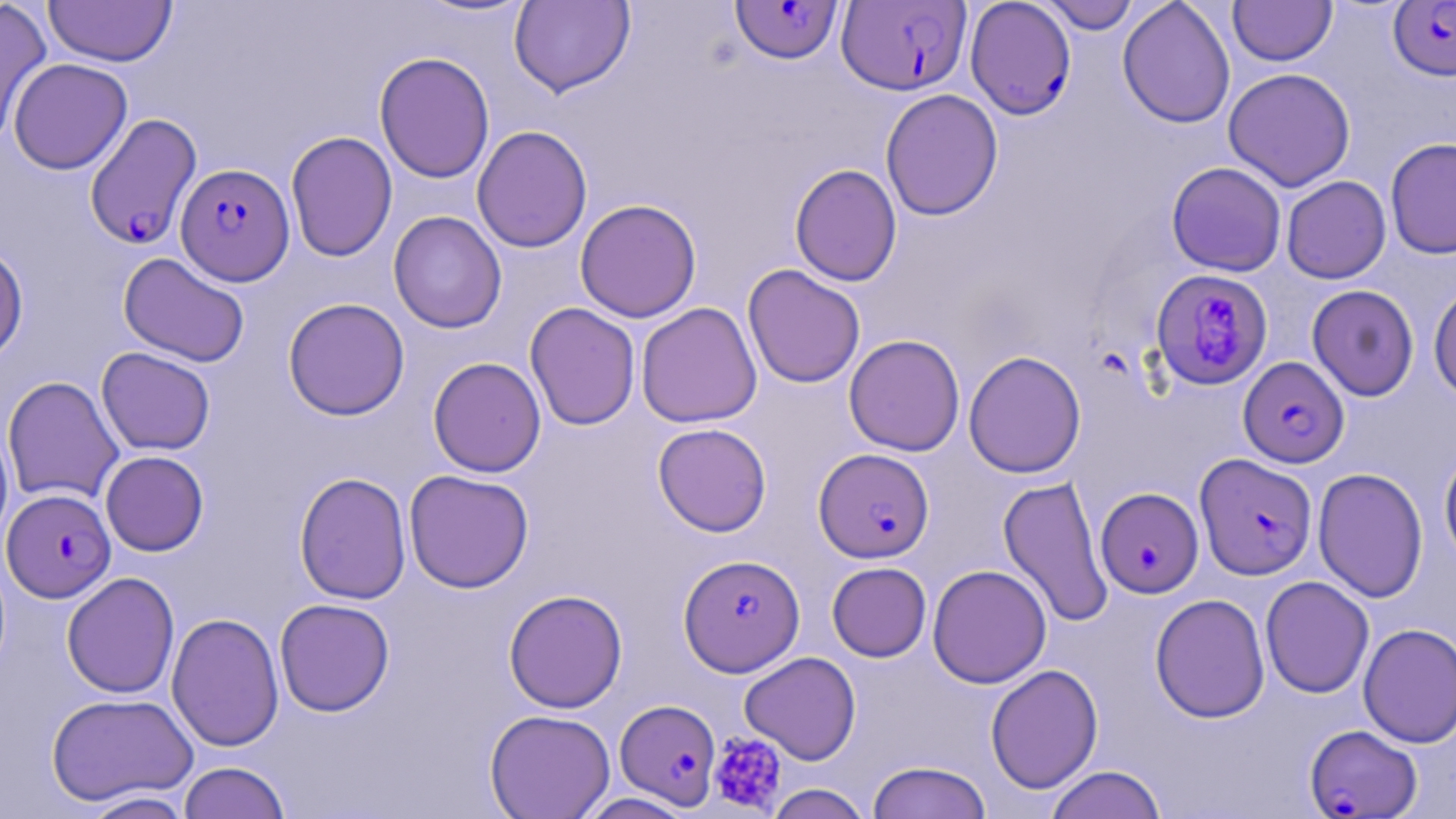

slide-level diagnosis = Plasmodium falciparum
platelet locations = approximate bounding boxes as named x1/y1/x2/y2 corners in pixels: (x1=708, y1=732, x2=787, y2=815)
field of view = one of a larger specimen
magnification = 1000x
image size = 1456×819 pixels
uninfected red blood cell locations = approximate bounding boxes as named x1/y1/x2/y2 corners in pixels: (x1=43, y1=0, x2=177, y2=67), (x1=413, y1=0, x2=537, y2=20), (x1=509, y1=0, x2=635, y2=97), (x1=1039, y1=0, x2=1141, y2=34), (x1=1117, y1=0, x2=1235, y2=129), (x1=1228, y1=0, x2=1336, y2=66), (x1=0, y1=3, x2=52, y2=145), (x1=374, y1=51, x2=495, y2=184), (x1=8, y1=58, x2=132, y2=174), (x1=1223, y1=67, x2=1356, y2=192), (x1=880, y1=88, x2=1003, y2=221), (x1=472, y1=125, x2=593, y2=253), (x1=285, y1=131, x2=398, y2=262), (x1=1385, y1=137, x2=1456, y2=259), (x1=1166, y1=161, x2=1287, y2=277), (x1=789, y1=163, x2=902, y2=286), (x1=1281, y1=176, x2=1391, y2=284), (x1=574, y1=199, x2=702, y2=323), (x1=388, y1=211, x2=507, y2=333), (x1=0, y1=242, x2=28, y2=366), (x1=118, y1=252, x2=250, y2=368), (x1=742, y1=264, x2=866, y2=388), (x1=1428, y1=283, x2=1456, y2=401), (x1=1307, y1=284, x2=1419, y2=401), (x1=282, y1=297, x2=410, y2=420), (x1=636, y1=302, x2=762, y2=428), (x1=524, y1=303, x2=641, y2=431), (x1=843, y1=334, x2=965, y2=456), (x1=96, y1=347, x2=216, y2=455), (x1=963, y1=350, x2=1086, y2=478), (x1=428, y1=356, x2=546, y2=477), (x1=2, y1=375, x2=124, y2=505), (x1=0, y1=419, x2=14, y2=550), (x1=652, y1=422, x2=772, y2=537), (x1=1439, y1=449, x2=1456, y2=571), (x1=100, y1=450, x2=209, y2=556), (x1=1313, y1=467, x2=1428, y2=603), (x1=404, y1=469, x2=534, y2=593), (x1=294, y1=472, x2=412, y2=605), (x1=998, y1=474, x2=1114, y2=629), (x1=827, y1=562, x2=931, y2=662), (x1=927, y1=564, x2=1052, y2=688), (x1=62, y1=572, x2=180, y2=698), (x1=1260, y1=576, x2=1374, y2=698), (x1=504, y1=589, x2=628, y2=713), (x1=1150, y1=593, x2=1270, y2=723), (x1=274, y1=598, x2=395, y2=716), (x1=166, y1=612, x2=284, y2=752), (x1=1358, y1=623, x2=1456, y2=748), (x1=739, y1=651, x2=861, y2=765), (x1=985, y1=663, x2=1103, y2=794), (x1=46, y1=692, x2=197, y2=806), (x1=484, y1=709, x2=616, y2=819), (x1=866, y1=760, x2=992, y2=819), (x1=178, y1=761, x2=290, y2=819), (x1=1044, y1=764, x2=1167, y2=819), (x1=764, y1=784, x2=873, y2=819), (x1=80, y1=791, x2=196, y2=818), (x1=575, y1=792, x2=696, y2=818)
stain = May-Grünwald-Giemsa
modality = optical microscopy
preparation = thin blood film
Plasmodium falciparum-infected red blood cell locations = approximate bounding boxes as named x1/y1/x2/y2 corners in pixels: (x1=730, y1=0, x2=844, y2=64), (x1=837, y1=0, x2=972, y2=97), (x1=965, y1=0, x2=1076, y2=120), (x1=1389, y1=1, x2=1456, y2=80), (x1=84, y1=113, x2=202, y2=249), (x1=176, y1=163, x2=294, y2=284), (x1=1150, y1=268, x2=1273, y2=390), (x1=1238, y1=356, x2=1349, y2=468), (x1=814, y1=448, x2=934, y2=563), (x1=1195, y1=453, x2=1318, y2=580), (x1=1096, y1=487, x2=1203, y2=598), (x1=2, y1=489, x2=116, y2=602), (x1=678, y1=554, x2=805, y2=676), (x1=615, y1=703, x2=717, y2=808), (x1=1305, y1=725, x2=1422, y2=818)